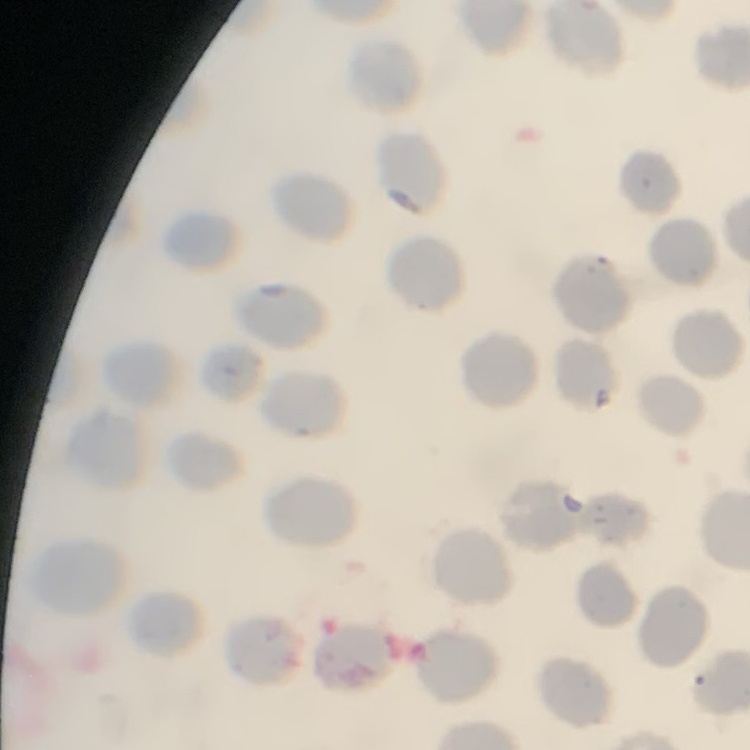
{
  "erythrocyte_morphology": "no rouleaux formation",
  "image_type": "one tile cut from a larger photomicrograph",
  "stain": "Field's or Giemsa",
  "preparation": "thin blood smear"
}